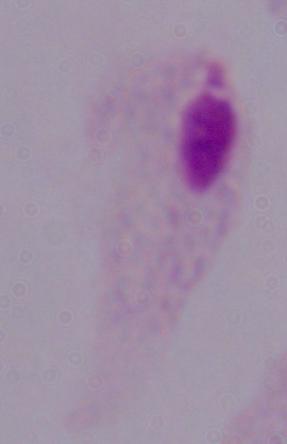

Summary:
  - Identification: trichomonad
  - Magnification: 1000x
  - Modality: photomicrograph